Outline each blood parasite and name the species.
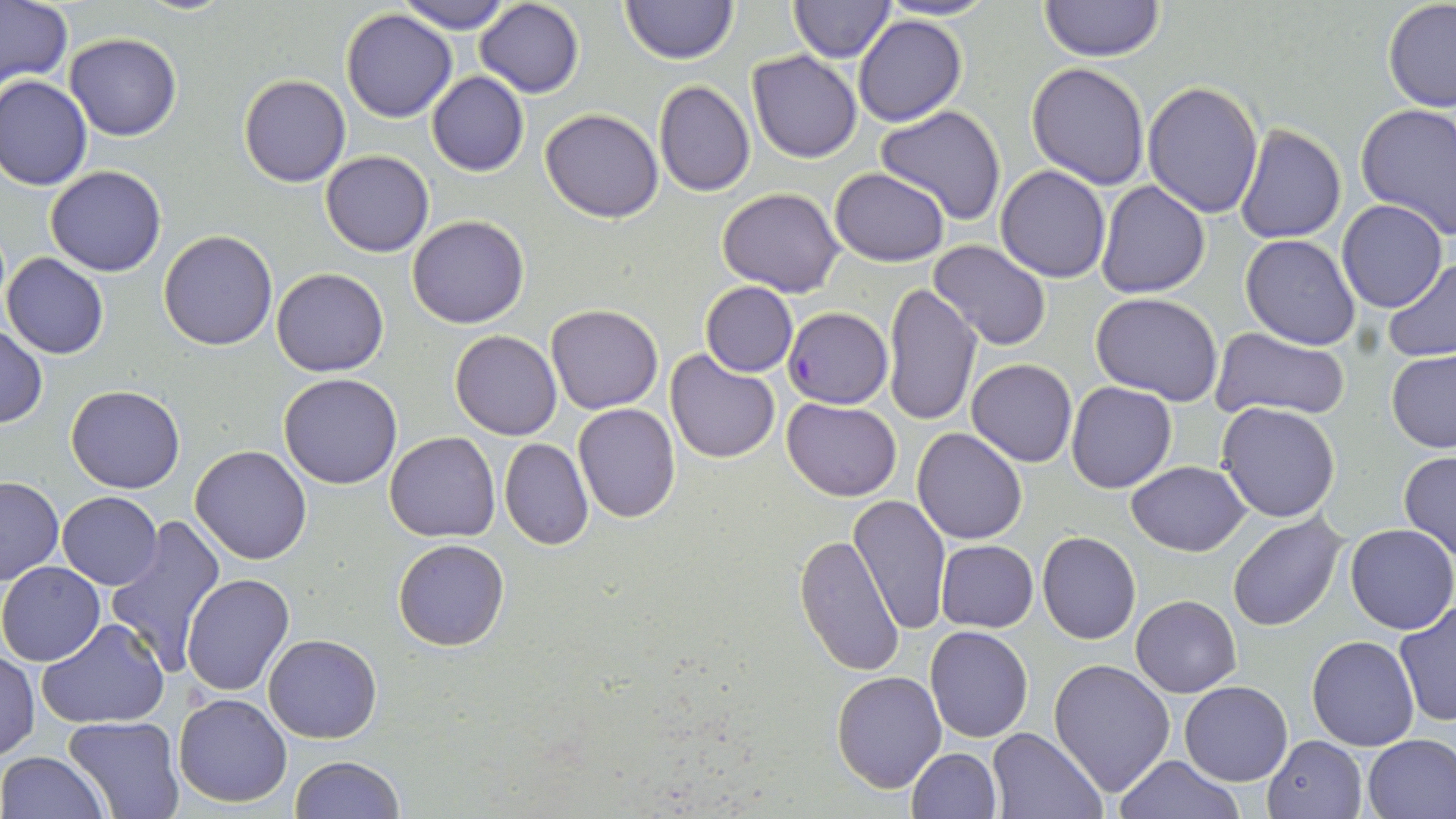
Approximate bounding boxes as [x1, y1, x2, y2] in pixels.
Plasmodium falciparum-infected red blood cells: [784, 308, 891, 407].
No Plasmodium ovale, Plasmodium malariae, Plasmodium vivax, Babesia divergens, or Trypanosoma brucei observed.

slide_level_diagnosis: Plasmodium falciparum
magnification: 1000x
modality: light microscopy
field_of_view: one of a larger specimen
preparation: thin blood smear
stain: May-Grünwald-Giemsa
uninfected_red_blood_cell_locations: 'approximate bounding boxes as [x1, y1, x2, y2] in pixels: [398, 0, 511, 33], [621, 0, 737, 66], [788, 0, 896, 63], [875, 0, 998, 21], [1038, 0, 1165, 64], [2, 1, 72, 88], [475, 1, 584, 98], [1382, 1, 1456, 112], [341, 7, 457, 122], [854, 14, 966, 127], [65, 32, 181, 141], [747, 51, 862, 164], [1026, 62, 1150, 188], [426, 71, 528, 176], [0, 75, 93, 191], [239, 75, 350, 187], [1142, 80, 1265, 218], [654, 81, 754, 197], [1355, 103, 1456, 239], [874, 107, 1006, 226], [540, 108, 664, 222], [1234, 125, 1346, 244], [319, 151, 434, 256], [994, 166, 1110, 283], [45, 167, 166, 277], [829, 168, 949, 266], [1095, 181, 1210, 299], [718, 186, 844, 296], [1336, 200, 1446, 312], [407, 215, 530, 329], [158, 230, 278, 350], [1241, 233, 1361, 350], [927, 238, 1053, 350], [3, 254, 110, 359], [1381, 257, 1456, 363], [272, 267, 388, 377], [701, 282, 798, 376], [882, 285, 983, 426], [1090, 293, 1223, 405], [546, 305, 665, 415], [446, 318, 659, 426], [0, 327, 47, 427], [1209, 328, 1354, 423], [450, 331, 561, 440], [665, 348, 780, 463], [1386, 349, 1456, 452], [968, 358, 1077, 468], [278, 373, 403, 489], [1066, 380, 1177, 493], [66, 385, 184, 494], [782, 397, 902, 502], [1216, 401, 1340, 522], [574, 402, 680, 521], [912, 428, 1027, 546], [385, 431, 500, 542], [498, 438, 594, 550], [189, 445, 313, 565], [1398, 450, 1456, 563], [1127, 460, 1252, 557], [1, 476, 63, 585], [58, 492, 163, 590], [849, 495, 952, 632], [105, 514, 227, 674], [1227, 514, 1348, 631], [1345, 523, 1456, 634], [1036, 531, 1140, 644], [796, 533, 903, 675], [393, 537, 509, 651], [936, 540, 1038, 633], [1, 560, 106, 666], [182, 572, 296, 695], [1131, 595, 1241, 697], [1394, 598, 1456, 729], [37, 620, 168, 728], [924, 626, 1033, 743], [264, 634, 382, 742], [1306, 637, 1419, 751], [1, 650, 39, 759], [1049, 658, 1177, 797], [830, 672, 946, 793], [1179, 681, 1292, 785], [172, 692, 291, 807], [63, 716, 182, 819], [988, 728, 1104, 818], [1262, 734, 1368, 818], [1360, 734, 1456, 818], [906, 748, 1001, 818], [0, 751, 108, 819], [289, 755, 405, 818], [1117, 755, 1243, 819]'
image_size: 1456×819 pixels